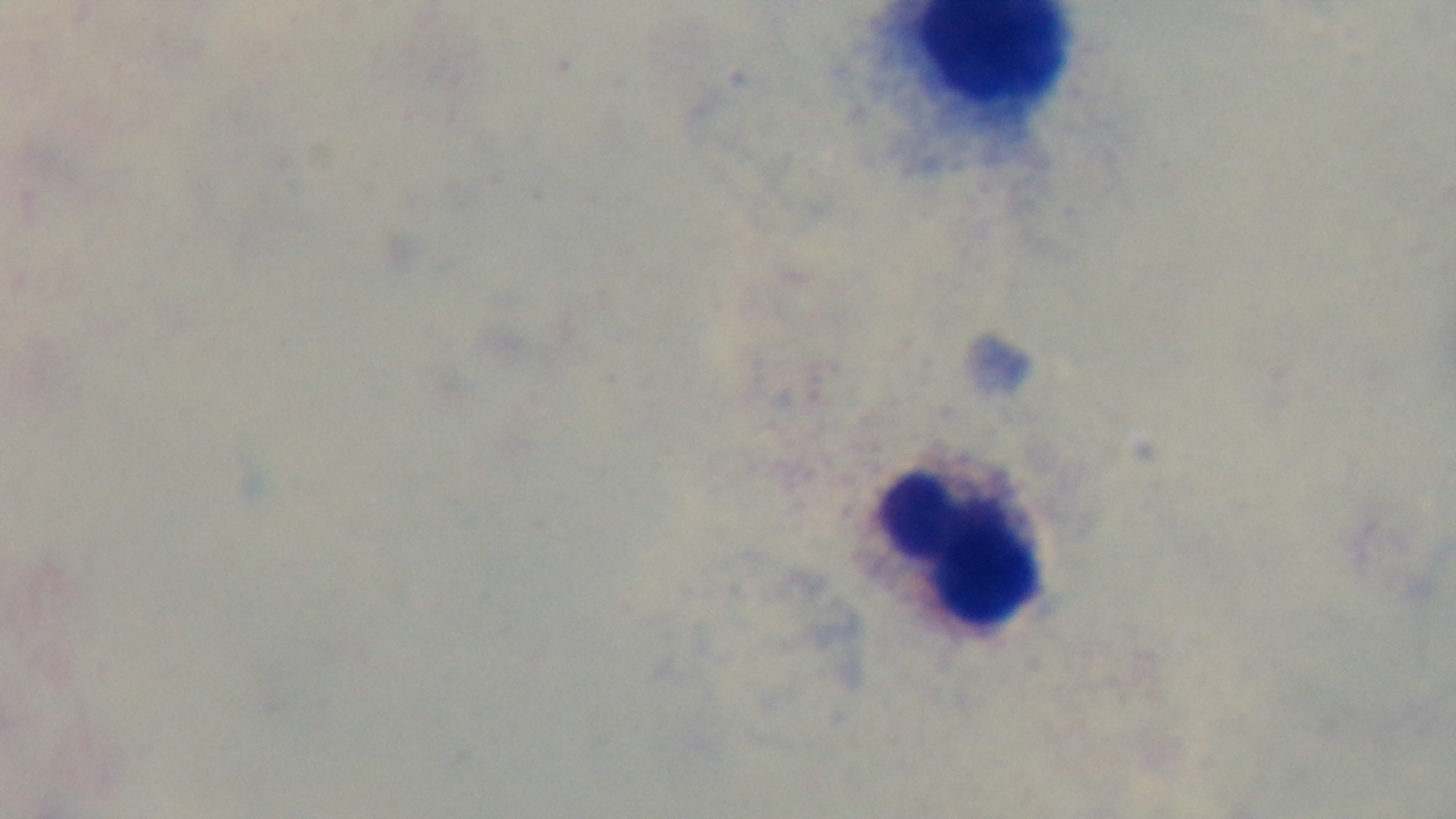
Oil-immersion objective, 100x. Light microscopy. Malaria status: uninfected. Preparation: thick blood film. One field from the slide. Giemsa stain. Captured with a mounted 4K digital camera.